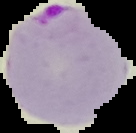
Summary:
  - Result: Plasmodium parasites identified
  - Image type: segmented cell region with the area outside set to black
  - Image size: 136×133 pixels
  - Preparation: thin blood smear